Report the malaria status of this cell.
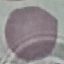

Uninfected.

Summary:
  - Preparation: thin smear
  - Stain: Giemsa
  - Image type: cell patch, automatically extracted from a larger field of view and resized to 64 × 64 pixels
  - Capture: smartphone through the microscope eyepiece